Give the extent of all Plasmodium ovale-infected red blood cells.
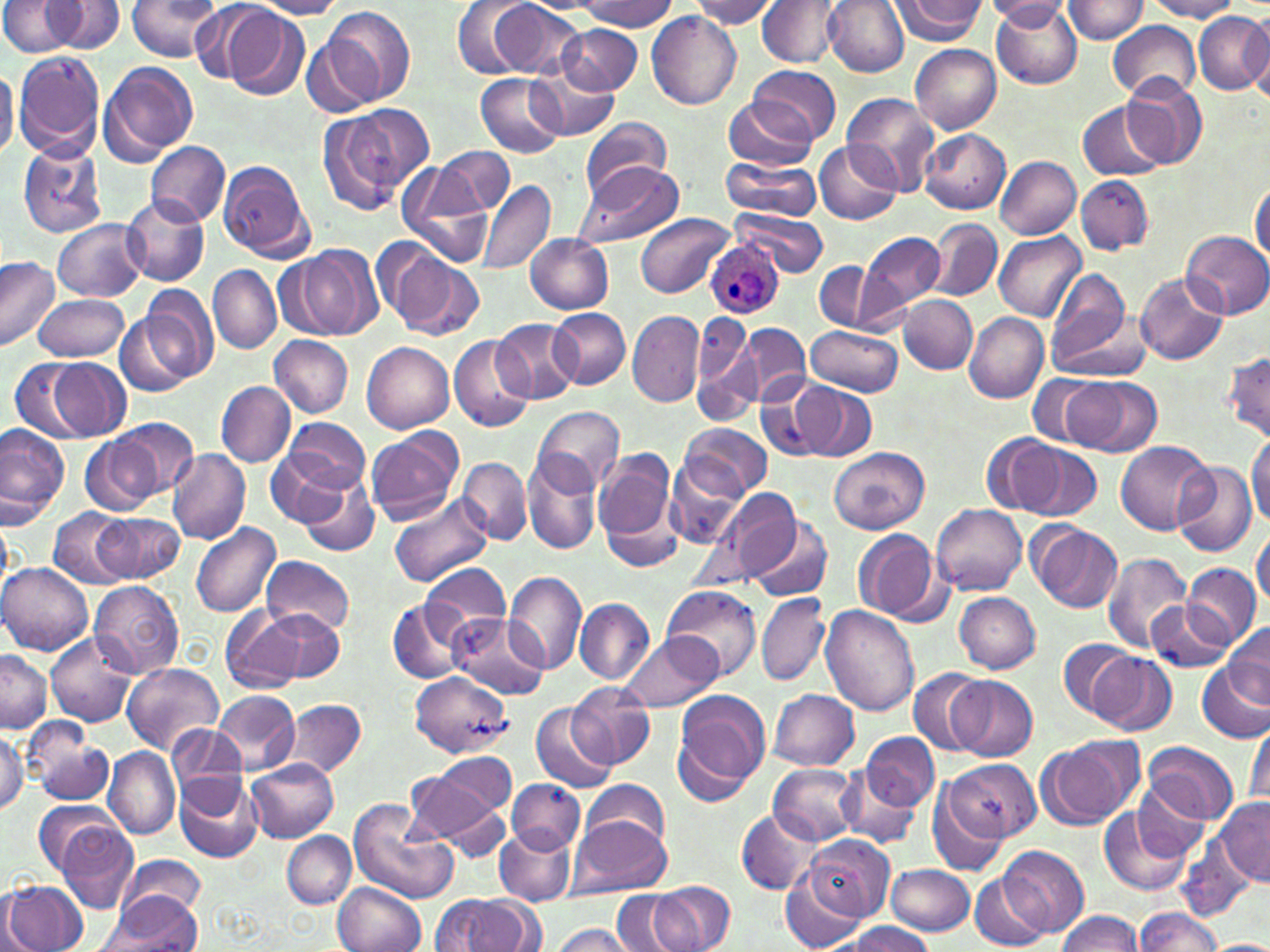

Approximate bounding boxes as (x1,y1)-(x2,y2) corner pairs in pixels.
Plasmodium ovale-infected red blood cells: (705,238)-(784,318).

Uninfected red blood cell locations: (126,0)-(223,63), (452,0)-(539,79), (575,0)-(679,32), (694,0)-(779,28), (758,0)-(843,67), (823,0)-(908,76), (889,0)-(985,43), (991,0)-(1082,90), (1064,0)-(1148,43), (1145,0)-(1241,21), (1,1)-(82,56), (46,1)-(126,54), (251,1)-(348,19), (487,1)-(582,79), (169,2)-(264,79), (984,2)-(1073,27), (323,5)-(415,104), (220,6)-(311,100), (1242,12)-(1269,101), (647,13)-(741,109), (1193,13)-(1268,95), (1108,21)-(1200,104), (557,24)-(641,96), (302,39)-(380,115), (911,44)-(1002,133), (13,51)-(105,161), (99,61)-(198,165), (747,64)-(840,147), (0,66)-(19,161), (530,66)-(620,141), (476,73)-(565,157), (1120,73)-(1210,170), (842,93)-(942,195), (723,95)-(817,170), (1078,100)-(1167,183), (317,107)-(416,216), (581,117)-(672,199), (919,128)-(1010,214), (814,140)-(903,226), (144,141)-(230,228), (18,143)-(108,239), (436,146)-(514,216), (995,156)-(1081,240), (719,159)-(823,221), (216,161)-(313,263), (572,161)-(686,248), (397,163)-(495,267), (1076,175)-(1153,254), (478,180)-(557,277), (1249,181)-(1269,267), (120,195)-(209,289), (732,207)-(828,276), (636,214)-(733,298), (926,218)-(1001,301), (54,219)-(148,301), (859,230)-(946,318), (1183,231)-(1270,317), (995,232)-(1085,320), (525,234)-(613,314), (379,243)-(484,341), (290,245)-(383,341), (0,256)-(59,352), (815,262)-(876,331), (208,265)-(282,353), (1044,269)-(1134,368), (1134,271)-(1229,367), (133,285)-(218,385), (33,294)-(130,362), (901,295)-(977,373), (549,309)-(630,389), (626,310)-(704,407), (115,312)-(195,399), (691,313)-(755,397), (965,313)-(1048,403), (491,318)-(582,403), (738,323)-(812,406), (807,325)-(902,395), (450,333)-(534,433), (270,335)-(353,417), (363,342)-(454,433), (692,343)-(762,425), (1221,351)-(1270,444), (11,356)-(96,443), (46,357)-(133,441), (1028,374)-(1106,447), (1071,378)-(1161,457), (217,381)-(295,467), (792,384)-(876,462), (759,386)-(828,461), (533,406)-(625,491), (110,416)-(198,501), (278,417)-(372,496), (0,423)-(68,527), (683,424)-(772,498), (366,426)-(462,524), (1247,431)-(1269,527), (981,435)-(1062,513), (81,436)-(161,515), (1116,440)-(1217,535), (263,443)-(363,533), (1012,444)-(1101,522), (830,445)-(929,533), (592,446)-(680,560), (168,449)-(250,545), (523,452)-(603,556), (664,456)-(746,547), (460,458)-(531,543), (1173,461)-(1257,558), (295,469)-(379,559), (714,488)-(799,581), (390,493)-(495,586), (933,503)-(1028,595), (49,508)-(134,590), (94,512)-(184,582), (0,515)-(12,591), (745,517)-(834,602), (1028,522)-(1124,613), (191,524)-(282,618), (1251,525)-(1269,608), (852,528)-(943,627), (1102,552)-(1194,653), (263,555)-(355,637), (1,563)-(94,655), (422,564)-(512,642), (1182,564)-(1260,650), (503,571)-(587,676), (90,580)-(183,677), (664,586)-(760,681), (754,591)-(830,687), (954,592)-(1041,674), (575,598)-(655,682), (388,599)-(472,685), (1145,599)-(1233,672), (221,604)-(306,693), (820,605)-(918,716), (255,610)-(346,685), (449,613)-(548,698), (1223,622)-(1269,706), (47,632)-(135,727), (615,632)-(724,713), (1057,639)-(1138,717), (0,650)-(52,732), (1091,652)-(1176,735), (1198,661)-(1270,743), (121,663)-(224,755), (909,666)-(988,756), (948,675)-(1037,761), (410,676)-(510,756), (568,683)-(655,767), (671,689)-(770,798), (769,689)-(860,770), (212,691)-(301,775), (284,698)-(367,779), (530,704)-(617,793), (1245,722)-(1270,811), (0,726)-(28,815), (167,729)-(247,806), (27,730)-(117,806), (861,732)-(938,809), (1036,734)-(1144,831), (1142,742)-(1236,825), (104,748)-(180,841), (433,752)-(517,814), (247,759)-(340,844), (945,759)-(1039,843), (770,764)-(862,844), (836,765)-(922,849), (405,768)-(503,848), (174,773)-(262,863), (507,779)-(583,852), (926,779)-(1011,878), (583,780)-(670,852), (1128,784)-(1214,867), (1214,797)-(1270,887), (32,798)-(118,876), (348,799)-(458,903), (437,804)-(512,862), (1100,807)-(1195,897), (736,810)-(821,893), (568,814)-(671,899), (51,817)-(139,914), (495,826)-(575,906), (283,832)-(356,907), (801,834)-(893,920), (1179,836)-(1253,921), (998,846)-(1088,937), (120,856)-(206,924), (885,864)-(973,934), (969,873)-(1053,950), (780,874)-(864,952), (5,881)-(89,952), (649,881)-(736,951), (334,882)-(426,952), (614,891)-(683,952), (101,893)-(203,952), (432,896)-(538,952), (1133,908)-(1225,950), (1057,911)-(1144,951), (548,922)-(637,952), (842,922)-(935,952), (1209,939)-(1270,952). Slide-level diagnosis: Plasmodium ovale. Image is 1270×952 pixels. 1000x magnification. May-Grünwald-Giemsa-stained preparation. Thin blood film. One field of a larger specimen. Light microscopy.